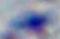 Photomicrograph. 1000x magnification. Toxoplasma gondii is seen.